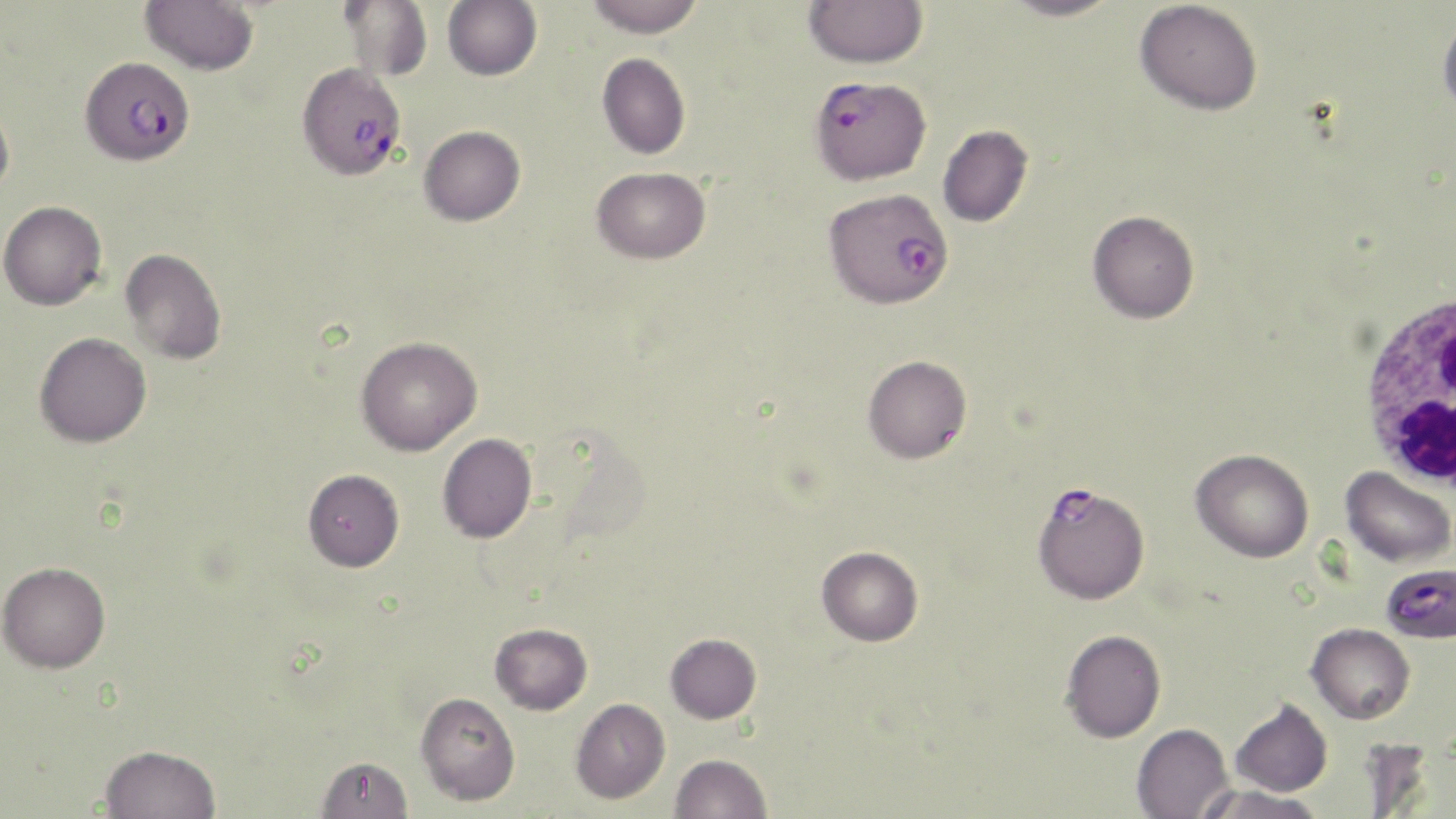

slide-level diagnosis = Plasmodium falciparum
uninfected red blood cell locations = approximate bounding boxes as (x1,y1)-(x2,y2) corner pairs in pixels: (140,0)-(259,75), (339,0)-(432,81), (443,0)-(542,81), (585,0)-(705,38), (1000,0)-(1120,21), (1135,0)-(1263,115), (804,1)-(928,67), (1437,13)-(1456,119), (597,53)-(691,158), (0,98)-(15,200), (937,124)-(1034,227), (419,125)-(526,225), (591,166)-(711,264), (0,201)-(107,310), (1087,210)-(1199,324), (120,248)-(226,364), (34,332)-(152,447), (356,337)-(482,455), (863,355)-(972,463), (437,433)-(537,543), (1190,448)-(1314,562), (1340,466)-(1455,568), (303,468)-(404,571), (816,546)-(924,646), (0,561)-(110,672), (490,623)-(592,715), (1306,623)-(1415,724), (1060,629)-(1166,742), (665,633)-(762,723), (415,692)-(521,806), (1229,697)-(1333,797), (570,698)-(670,804), (1131,722)-(1234,819), (99,744)-(220,819), (670,753)-(772,819), (315,756)-(414,818), (1192,784)-(1326,819)
modality = optical microscopy
field of view = one of a larger specimen
preparation = thin blood film
stain = May-Grünwald-Giemsa
image size = 1456×819 pixels
white blood cell locations = approximate bounding boxes as (x1,y1)-(x2,y2) corner pairs in pixels: (1354,287)-(1456,495)
Plasmodium falciparum-infected red blood cell locations = approximate bounding boxes as (x1,y1)-(x2,y2) corner pairs in pixels: (82,58)-(197,164), (307,66)-(409,180), (810,75)-(931,186), (824,188)-(954,309), (1040,486)-(1150,607), (1381,562)-(1456,645)
magnification = 1000x